Report the malaria status of this cell.
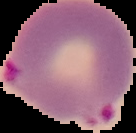

Parasitized.

preparation = thin blood smear
image size = 136×133 pixels
image type = segmented cell region on a black background